Classify this cell by malaria status.
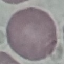
Uninfected.

Summary:
  - Image type: automatically extracted cell patch, resized to 64 × 64 pixels
  - Capture: smartphone through the microscope eyepiece
  - Stain: Giemsa
  - Preparation: thin blood smear